Look for parasitized red blood cells.
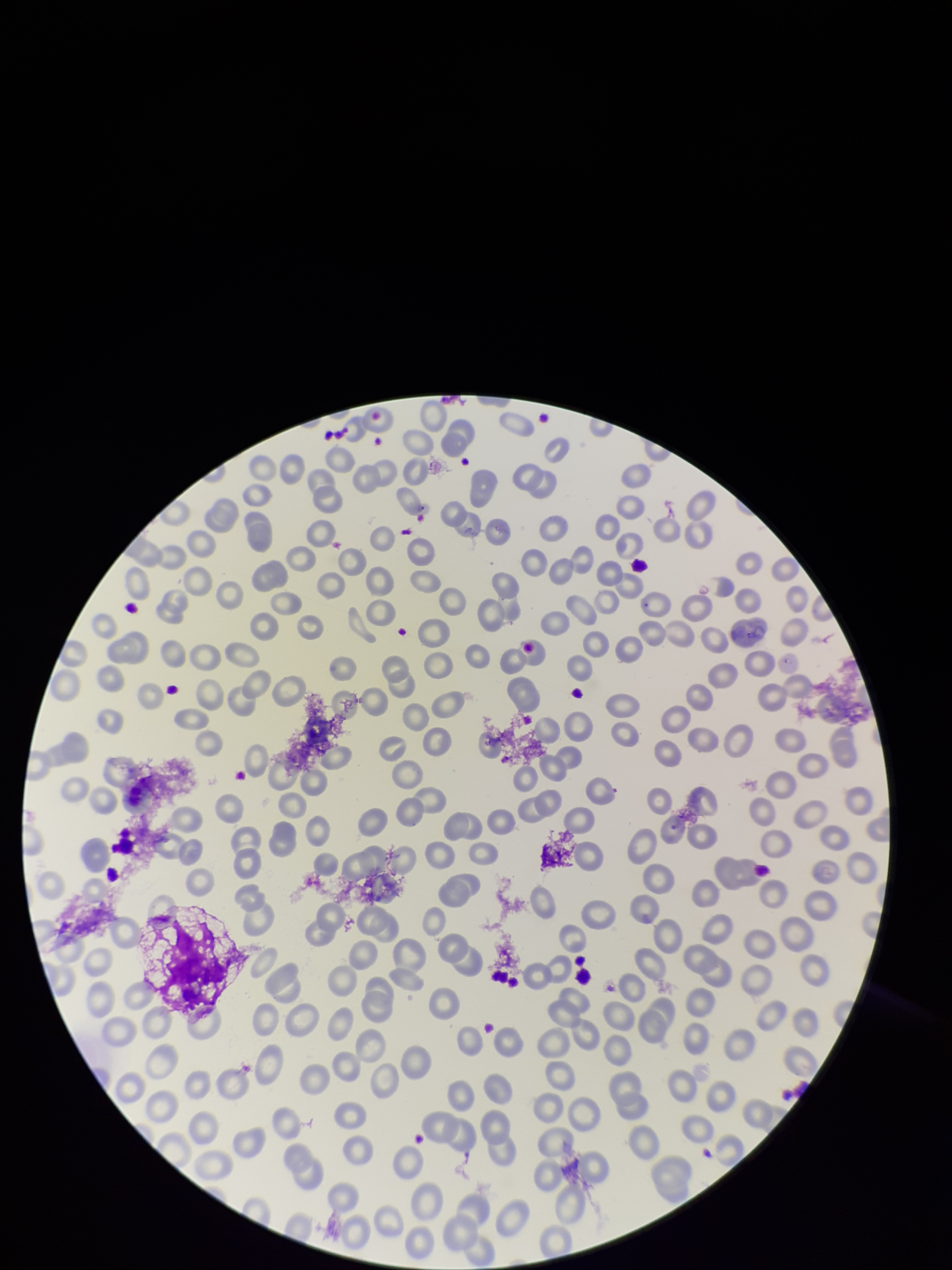

None seen.

Smartphone photograph taken through the eyepiece of a microscope. Parasitized red blood cell count: 0. Species reported for this patient: Plasmodium falciparum. Preparation: thin smear. Red blood cell count: 226. Stained with Giemsa. Image is 952×1270 pixels. One field from this slide. Patient malaria status: infected.